Point out cells.
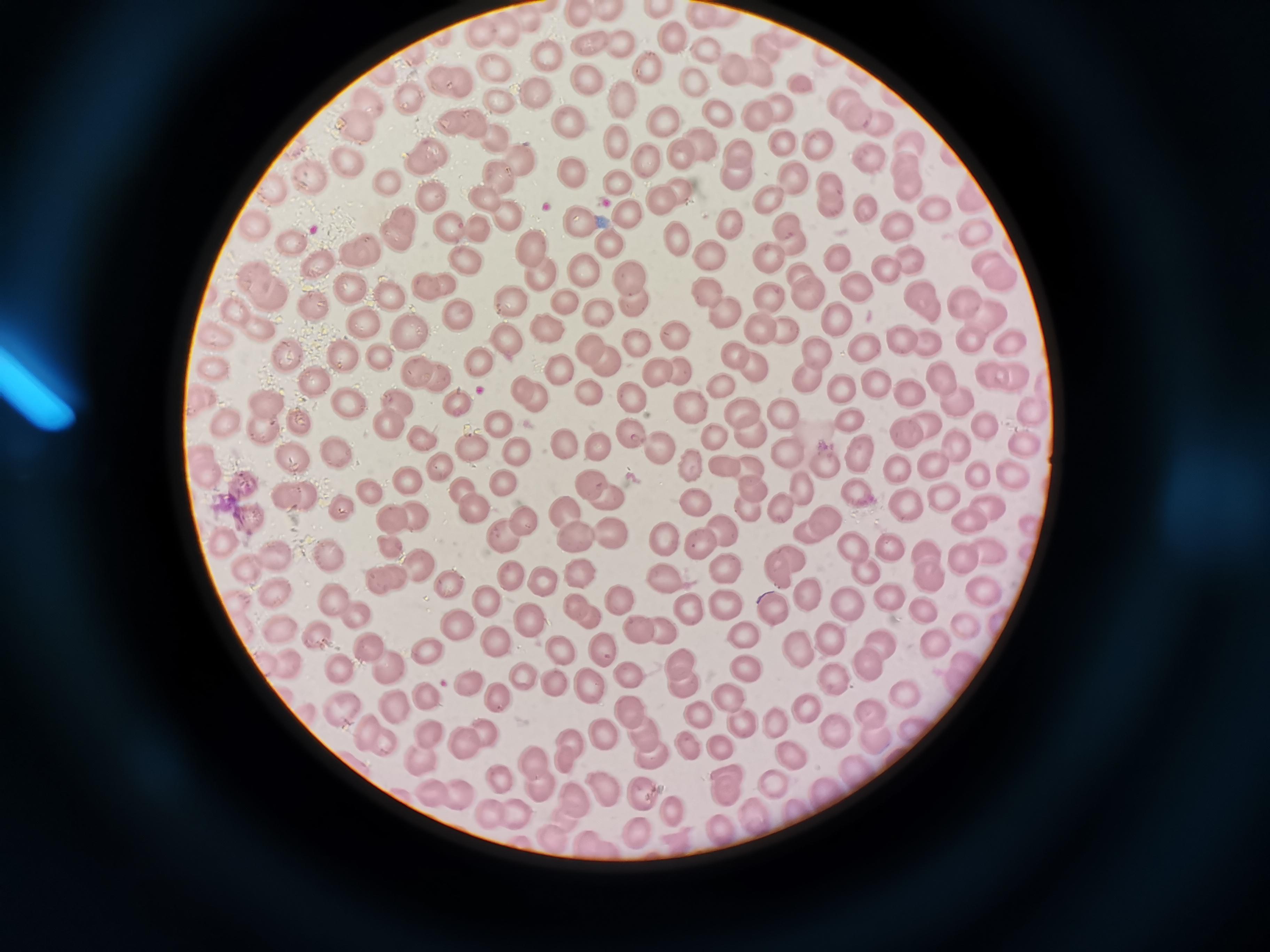

Approximate centers as [x, y] in pixels.
Cells: [591, 45], [621, 47], [545, 56], [493, 66], [650, 68], [585, 76], [694, 81], [436, 83], [462, 84], [539, 90], [410, 99], [841, 100], [502, 102], [626, 102], [368, 103], [778, 106], [717, 108], [664, 117], [755, 117], [570, 119], [877, 120], [458, 123], [356, 129], [495, 139], [815, 141], [614, 142], [785, 143], [910, 144], [737, 153], [680, 154], [428, 158], [350, 159], [519, 159], [649, 161], [871, 162], [905, 163], [566, 169], [502, 172], [731, 175], [313, 179], [792, 179], [386, 180], [611, 180], [827, 182], [681, 186], [907, 187], [280, 192], [433, 195], [768, 199], [482, 201], [659, 201], [832, 208], [866, 209], [935, 209], [624, 214], [508, 220], [580, 220], [256, 224], [786, 225], [453, 226], [896, 226], [726, 227], [480, 230], [398, 232], [977, 232], [288, 239], [680, 239], [531, 245], [605, 246], [790, 246], [353, 247], [708, 252], [765, 253], [833, 254], [464, 258], [910, 258], [316, 264], [582, 268], [994, 268], [889, 269], [539, 271], [801, 274], [625, 278], [349, 283], [430, 284], [266, 285], [709, 290], [853, 290], [811, 292], [391, 295], [768, 297], [963, 298], [512, 301], [927, 301], [561, 303], [634, 306], [314, 308], [457, 310], [594, 312], [248, 313], [837, 317], [991, 319], [366, 320], [759, 323], [405, 324], [548, 327], [787, 332], [503, 336], [677, 337], [968, 338], [896, 339], [1010, 339], [222, 340], [634, 340], [927, 341], [590, 349], [864, 349], [289, 354], [813, 354], [345, 355], [382, 355], [731, 358], [479, 361], [755, 363], [605, 365], [215, 369], [559, 370], [414, 371], [654, 371], [1001, 371], [940, 372], [678, 374], [440, 375], [803, 376], [317, 380], [877, 381], [721, 384], [525, 387], [839, 387], [911, 388], [590, 394], [351, 395], [632, 396], [204, 397], [397, 398], [263, 403], [537, 403], [458, 404], [690, 404], [737, 405], [960, 405], [780, 412], [1035, 417], [300, 419], [853, 420], [223, 422], [391, 422], [498, 425], [924, 425], [262, 427], [747, 427], [987, 427], [904, 432], [635, 435], [421, 436], [711, 438], [564, 441], [466, 443], [596, 443], [1022, 443], [333, 445], [666, 449], [515, 450], [788, 450], [958, 450], [856, 451], [294, 454], [691, 459], [205, 460], [723, 462], [898, 462], [748, 463], [439, 464], [827, 466], [936, 466], [1010, 473], [978, 479], [409, 480], [587, 481], [504, 485], [751, 486], [799, 487], [247, 488], [857, 489], [463, 490], [371, 492], [607, 492], [296, 495], [697, 497], [940, 500], [782, 501], [901, 503], [470, 507], [566, 509], [349, 510], [987, 510], [751, 511], [419, 516], [252, 519], [394, 519], [822, 519], [963, 519], [525, 521], [722, 525], [612, 530], [807, 532], [575, 534], [664, 537], [700, 542], [230, 545], [390, 545], [846, 545], [889, 546], [924, 548], [276, 554], [324, 555], [963, 560], [416, 565], [785, 565], [245, 567], [725, 569], [864, 569], [578, 570], [512, 571], [386, 577], [663, 577], [446, 579], [542, 580], [930, 580], [982, 589], [277, 590], [486, 595], [336, 596], [621, 596], [809, 597], [889, 602], [724, 603], [846, 603], [581, 605], [772, 607], [917, 610], [689, 611], [357, 613], [533, 616], [462, 621], [639, 624], [964, 625], [277, 626], [659, 628], [738, 631], [312, 632], [831, 635], [494, 638], [880, 640], [937, 641], [365, 643], [557, 645], [429, 647], [601, 647], [797, 648], [284, 662], [339, 663], [684, 663], [865, 665], [741, 666], [387, 668], [523, 675], [630, 676], [833, 676], [551, 680], [587, 680], [466, 681], [685, 684], [723, 693], [498, 694], [902, 695], [429, 697], [396, 702], [337, 706], [806, 707], [630, 711], [867, 711], [693, 713], [774, 718], [741, 722], [483, 727], [362, 728], [641, 730], [831, 731], [429, 732], [876, 733], [601, 734], [567, 736], [383, 740], [461, 740], [687, 742], [722, 744], [418, 754], [791, 754], [652, 755], [534, 757], [564, 757], [855, 766], [499, 777], [536, 779], [773, 782], [733, 784], [600, 786], [641, 788], [425, 789], [828, 789], [459, 794], [570, 795], [795, 807], [512, 808], [673, 809], [486, 811], [752, 817], [715, 826], [641, 829], [554, 830].

Summary:
  - Field of view: single
  - Image size: 1270×952 pixels
  - Stain: Giemsa
  - Capture: smartphone camera at the microscope eyepiece
  - Preparation: thin blood film